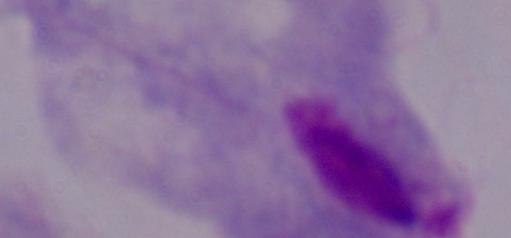

1000x magnification. Micrograph. A trichomonad is seen.